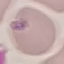 Result: no malaria parasites seen. Cell patch, automatically extracted from a larger field of view and resized to 64 × 64 pixels. Thin blood film. Giemsa-stained preparation. Acquired by smartphone through the microscope eyepiece.